Comment on the morphology of the erythrocytes.
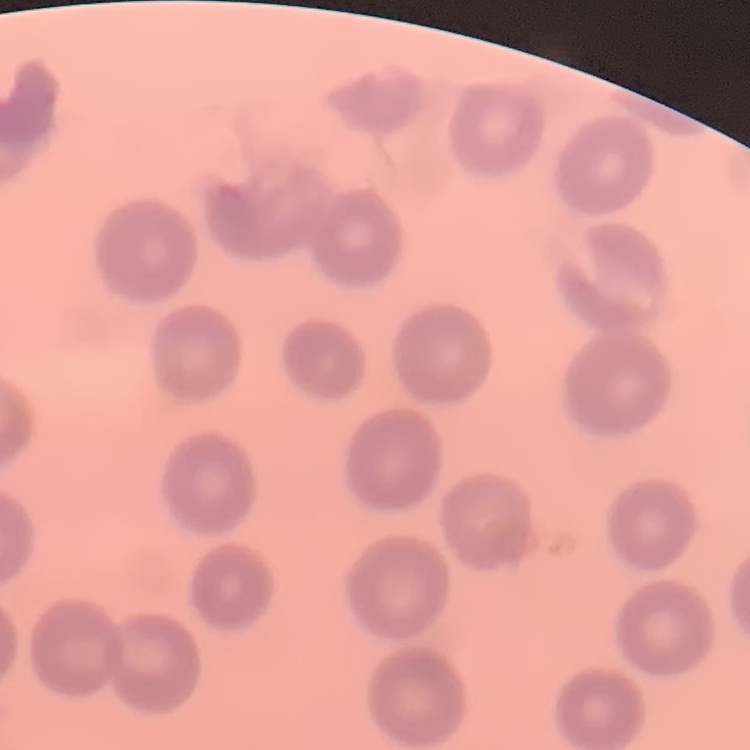

They show no rouleaux formation.

image_type: square crop of a larger photomicrograph
stain: Field's or Giemsa
preparation: thin blood smear